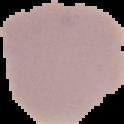
Summary:
  - Preparation: thin blood smear
  - Malaria status: uninfected
  - Image size: 124×124 pixels
  - Image type: segmented cell region on a black background